Assess this cell for malaria.
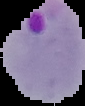
Parasitized.

{
  "image_size": "85×106 pixels",
  "preparation": "thin blood film",
  "image_type": "segmented cell region with the area outside set to black"
}